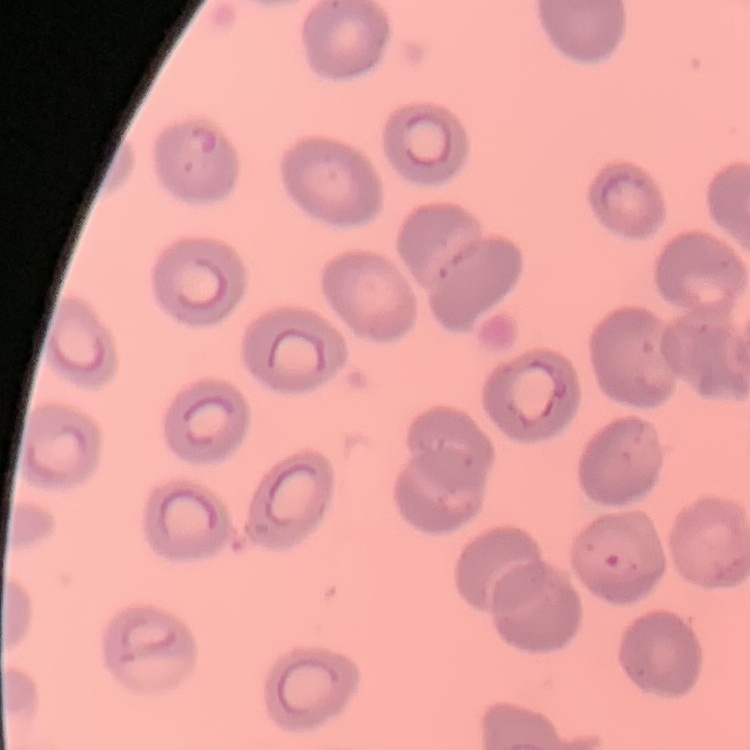

The red blood cells show no rouleaux formation. Thin peripheral smear. Stained with either Field's or Giemsa. Square crop of a larger photomicrograph.